Outline each Plasmodium falciparum-infected red blood cell.
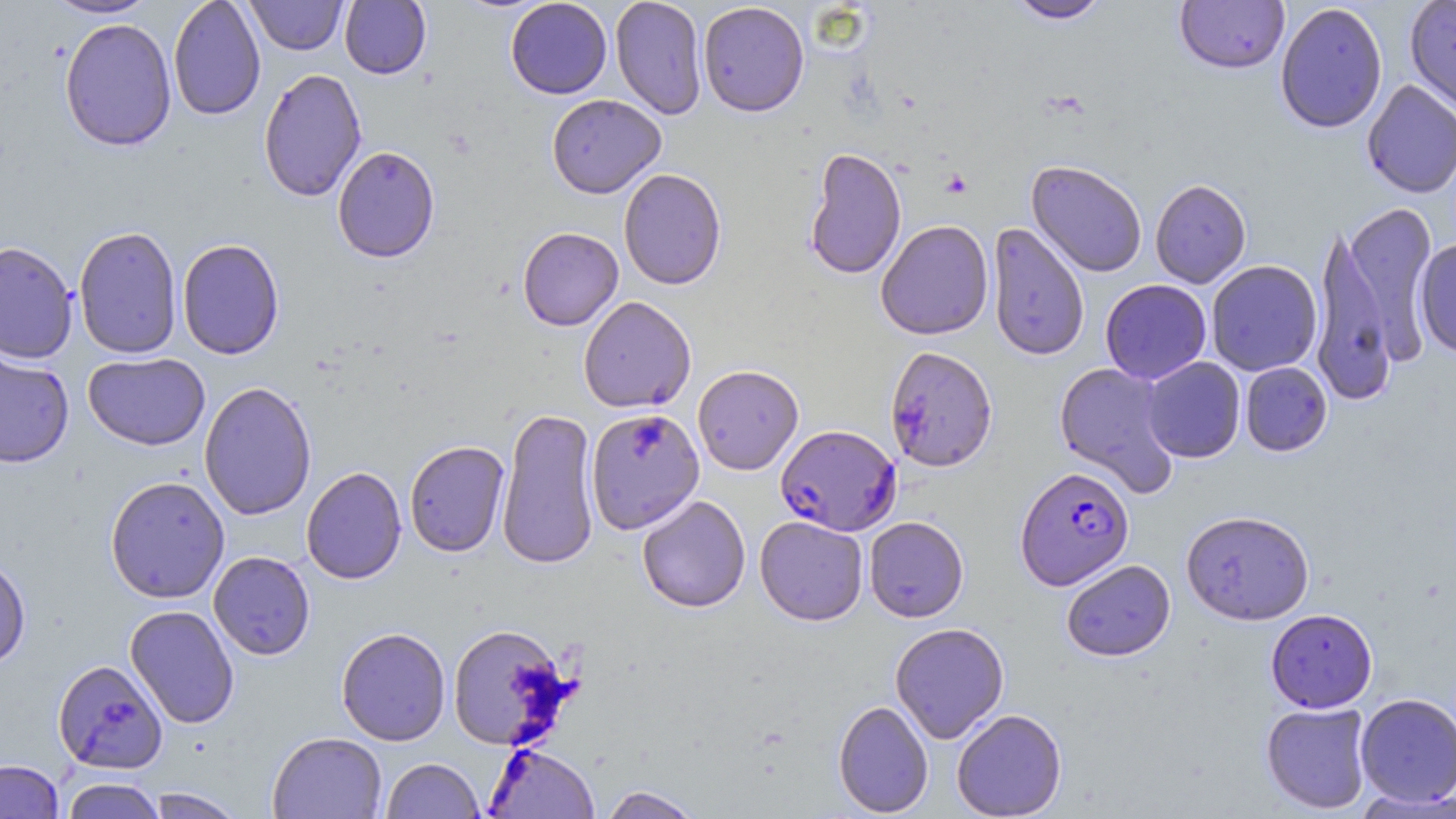

Approximate bounding boxes as [x1, y1, x2, y2] in pixels.
Plasmodium falciparum-infected red blood cells: [775, 424, 901, 535], [1015, 465, 1134, 590].

Summary:
  - Uninfected red blood cell locations: [45, 0, 157, 19], [168, 0, 266, 120], [246, 0, 348, 55], [505, 0, 612, 99], [610, 0, 707, 119], [1005, 0, 1113, 24], [1174, 0, 1290, 74], [1404, 0, 1456, 115], [339, 1, 432, 79], [697, 1, 809, 116], [1275, 2, 1388, 134], [59, 17, 177, 151], [258, 68, 367, 202], [1362, 80, 1456, 199], [547, 94, 666, 198], [332, 145, 440, 263], [804, 147, 907, 279], [1026, 160, 1147, 278], [619, 168, 726, 289], [1150, 178, 1251, 288], [1312, 199, 1437, 401], [876, 219, 994, 340], [986, 222, 1089, 362], [74, 225, 183, 359], [517, 227, 623, 330], [177, 238, 285, 360], [1414, 238, 1456, 360], [0, 241, 78, 363], [1206, 260, 1322, 376], [1100, 279, 1212, 384], [578, 296, 696, 413], [884, 345, 998, 473], [0, 349, 75, 469], [83, 352, 210, 450], [1141, 357, 1245, 463], [1054, 362, 1181, 498], [1240, 362, 1332, 456], [692, 364, 804, 475], [199, 381, 317, 520], [495, 407, 600, 570], [586, 408, 705, 533], [405, 440, 510, 557], [301, 466, 406, 585], [105, 475, 230, 603], [637, 494, 751, 613], [1181, 509, 1314, 625], [754, 515, 869, 626], [864, 516, 969, 622], [208, 551, 315, 660], [0, 554, 31, 670], [1061, 559, 1175, 661], [124, 604, 240, 729], [1266, 608, 1378, 713], [890, 622, 1009, 743], [447, 624, 575, 751], [336, 627, 451, 746], [53, 659, 168, 774], [1354, 693, 1456, 807], [833, 700, 934, 817], [1261, 703, 1373, 814], [952, 708, 1067, 818], [267, 731, 387, 818], [486, 742, 599, 818], [381, 758, 484, 819], [0, 759, 64, 819], [60, 776, 166, 819], [597, 785, 704, 819], [144, 787, 247, 818]
  - Slide-level diagnosis: Plasmodium falciparum
  - Field of view: single
  - Magnification: 1000x
  - Image size: 1456×819 pixels
  - Preparation: thin blood smear
  - Modality: optical microscopy
  - Stain: May-Grünwald-Giemsa